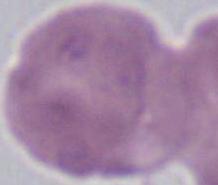

modality = micrograph
magnification = 1000x
identification = erythrocyte